Name the blood parasite species.
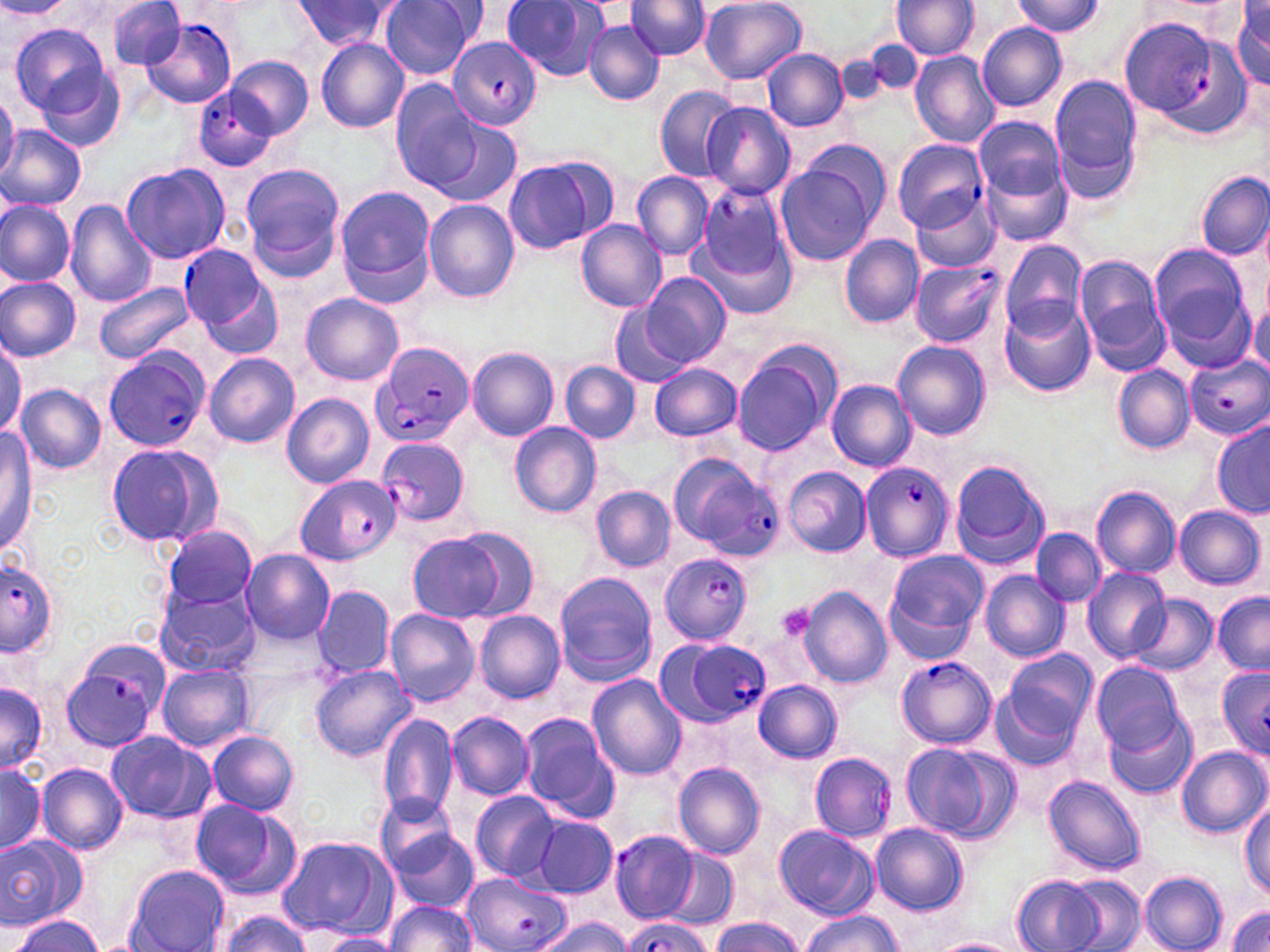
Plasmodium falciparum.

{
  "magnification": "1000x",
  "image_size": "1270×952 pixels",
  "preparation": "thin blood smear",
  "modality": "optical microscopy",
  "stain": "May-Grünwald-Giemsa",
  "platelet_locations": "approximate bounding boxes as [x1, y1, x2, y2] in pixels: [776, 603, 816, 644]",
  "uninfected_red_blood_cell_locations": "approximate bounding boxes as [x1, y1, x2, y2] in pixels: [108, 0, 187, 72], [380, 0, 477, 80], [500, 0, 609, 83], [628, 0, 710, 61], [700, 0, 807, 84], [1012, 0, 1105, 37], [0, 1, 70, 19], [290, 1, 401, 52], [891, 1, 979, 60], [1229, 1, 1270, 91], [584, 20, 664, 106], [976, 22, 1069, 112], [10, 24, 116, 124], [315, 37, 410, 133], [860, 40, 925, 92], [763, 48, 848, 131], [910, 51, 1001, 148], [32, 52, 128, 154], [834, 53, 895, 113], [227, 57, 313, 139], [1049, 77, 1142, 200], [390, 82, 483, 192], [654, 86, 741, 181], [0, 91, 19, 184], [701, 102, 797, 200], [973, 116, 1067, 207], [432, 117, 522, 208], [0, 125, 87, 211], [802, 138, 890, 223], [976, 142, 1076, 251], [502, 156, 613, 256], [121, 162, 230, 265], [240, 162, 345, 272], [775, 164, 878, 266], [632, 172, 713, 259], [1196, 172, 1269, 259], [334, 185, 438, 303], [912, 193, 1003, 273], [0, 200, 74, 286], [66, 200, 157, 308], [423, 200, 520, 302], [577, 218, 668, 311], [700, 236, 794, 319], [840, 236, 923, 328], [998, 240, 1089, 336], [1149, 244, 1253, 353], [1074, 254, 1170, 370], [642, 273, 730, 368], [0, 276, 82, 361], [93, 282, 196, 364], [302, 293, 403, 386], [999, 298, 1095, 397], [609, 301, 692, 387], [1247, 302, 1269, 380], [893, 340, 991, 440], [0, 343, 22, 437], [731, 344, 838, 455], [467, 347, 559, 440], [205, 352, 299, 448], [829, 359, 985, 459], [560, 361, 640, 444], [648, 363, 742, 440], [1112, 365, 1194, 454], [826, 379, 916, 471], [15, 383, 106, 474], [281, 394, 374, 487], [509, 421, 602, 517], [1213, 421, 1270, 518], [0, 429, 36, 552], [104, 442, 223, 549], [949, 459, 1051, 571], [784, 466, 872, 558], [591, 485, 675, 573], [1091, 486, 1180, 578], [1173, 505, 1265, 590], [162, 525, 256, 610], [449, 527, 540, 620], [1030, 528, 1106, 606], [409, 535, 503, 621], [240, 548, 335, 645], [883, 551, 988, 659], [1082, 567, 1171, 663], [980, 570, 1072, 661], [554, 572, 659, 684], [153, 583, 260, 677], [313, 585, 395, 680], [798, 587, 892, 688], [1213, 592, 1270, 674], [1130, 595, 1218, 676], [385, 608, 480, 707], [474, 610, 565, 704], [994, 649, 1097, 759], [1090, 661, 1187, 756], [156, 664, 255, 752], [311, 666, 415, 761], [587, 674, 688, 780], [754, 679, 843, 764], [0, 682, 47, 772], [1104, 705, 1197, 799], [447, 712, 534, 799], [518, 712, 618, 819], [377, 714, 460, 820], [207, 730, 301, 815], [106, 731, 214, 823], [897, 740, 1016, 843], [1178, 747, 1268, 838], [0, 761, 47, 858], [673, 761, 766, 859], [36, 763, 128, 856], [1043, 777, 1144, 876], [470, 790, 562, 881], [375, 794, 464, 879], [188, 797, 301, 901], [1240, 800, 1270, 896], [532, 817, 618, 897], [871, 822, 969, 915], [382, 823, 480, 912], [774, 825, 877, 919], [0, 833, 88, 929], [277, 835, 396, 938], [662, 849, 738, 931], [125, 866, 228, 951], [1140, 871, 1228, 952], [1012, 875, 1104, 952], [1063, 875, 1145, 951], [383, 901, 477, 952], [1227, 904, 1270, 952], [213, 912, 313, 952], [798, 912, 902, 952], [9, 914, 103, 951], [532, 917, 634, 952], [709, 917, 804, 952], [317, 931, 401, 952], [931, 937, 1025, 952]",
  "field_of_view": "one of a larger specimen",
  "plasmodium_falciparum_infected_red_blood_cell_locations": "approximate bounding boxes as [x1, y1, x2, y2] in pixels: [141, 16, 238, 109], [1118, 17, 1232, 122], [446, 35, 542, 131], [197, 72, 295, 169], [893, 139, 988, 232], [696, 184, 790, 289], [181, 247, 281, 353], [911, 260, 1005, 347], [371, 341, 474, 447], [102, 346, 211, 454], [1185, 351, 1270, 440], [376, 437, 470, 528], [666, 454, 778, 589], [861, 461, 953, 562], [295, 475, 401, 565], [659, 552, 753, 644], [0, 561, 58, 656], [663, 636, 772, 725], [61, 639, 169, 750], [895, 655, 996, 750], [1217, 665, 1270, 757], [809, 752, 897, 842], [608, 829, 699, 924], [461, 871, 568, 952], [616, 917, 713, 952]"
}